Outline each uninfected red blood cell.
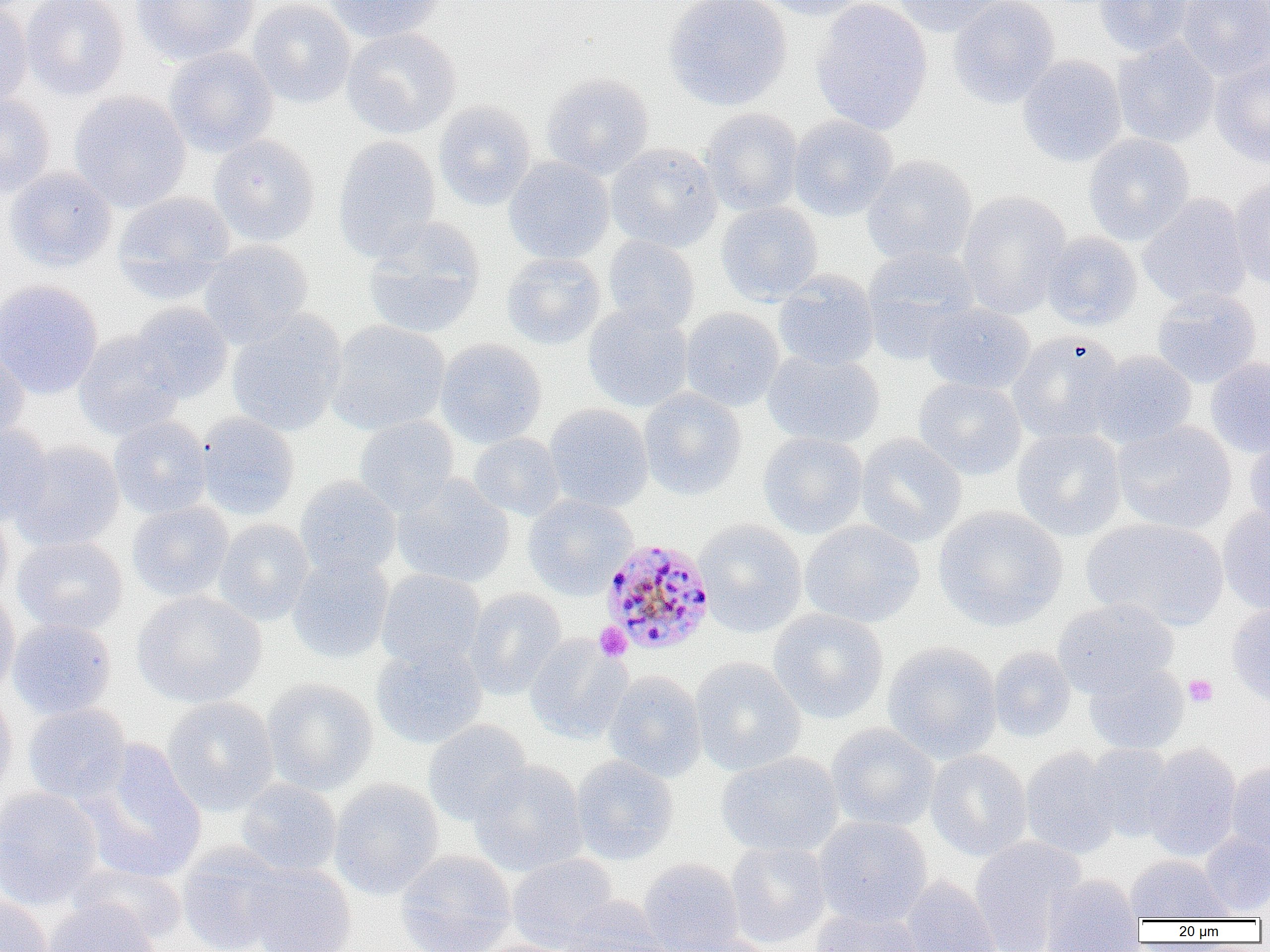

Approximate bounding boxes as [x1, y1, x2, y2] in pixels.
Uninfected red blood cells: [21, 0, 130, 101], [131, 0, 261, 65], [248, 0, 357, 108], [321, 0, 442, 43], [663, 0, 793, 111], [756, 0, 871, 21], [810, 0, 933, 135], [890, 0, 1009, 37], [948, 0, 1060, 108], [1093, 0, 1197, 57], [1176, 0, 1269, 79], [0, 2, 33, 109], [341, 27, 462, 139], [1112, 38, 1220, 148], [164, 46, 278, 157], [1018, 55, 1126, 167], [1210, 55, 1270, 168], [541, 72, 654, 179], [68, 91, 191, 212], [0, 94, 55, 199], [433, 100, 537, 211], [700, 107, 804, 216], [787, 115, 898, 221], [1083, 133, 1194, 245], [208, 134, 321, 247], [333, 135, 442, 261], [605, 143, 723, 252], [862, 154, 978, 266], [504, 156, 614, 265], [3, 166, 117, 273], [1230, 175, 1270, 288], [957, 190, 1072, 319], [113, 191, 236, 300], [1138, 193, 1252, 310], [716, 201, 823, 305], [362, 217, 486, 339], [1041, 231, 1142, 330], [602, 235, 700, 333], [198, 240, 313, 347], [862, 246, 980, 362], [501, 253, 606, 350], [773, 270, 880, 371], [0, 279, 103, 399], [1151, 289, 1261, 388], [128, 301, 234, 403], [922, 302, 1035, 394], [583, 304, 694, 413], [680, 307, 785, 411], [226, 309, 347, 437], [327, 320, 450, 435], [73, 330, 185, 440], [1007, 331, 1125, 444], [435, 339, 547, 448], [0, 342, 30, 444], [1089, 350, 1197, 449], [762, 351, 885, 448], [1205, 357, 1270, 458], [913, 377, 1027, 480], [638, 387, 747, 500], [544, 404, 653, 512], [195, 412, 300, 520], [353, 415, 460, 515], [109, 416, 212, 519], [1112, 421, 1237, 534], [0, 422, 54, 525], [1011, 428, 1127, 542], [1243, 430, 1270, 537], [757, 432, 869, 539], [468, 433, 565, 520], [856, 433, 967, 547], [9, 441, 125, 551], [392, 475, 515, 588], [294, 476, 401, 580], [523, 494, 636, 599], [127, 501, 234, 602], [0, 502, 13, 608], [1218, 503, 1270, 615], [933, 505, 1067, 631], [1081, 517, 1228, 630], [213, 519, 314, 625], [695, 519, 807, 637], [799, 520, 925, 628], [12, 535, 128, 635], [287, 554, 394, 663], [376, 569, 486, 671], [466, 588, 567, 699], [0, 590, 20, 702], [133, 591, 266, 708], [1053, 598, 1178, 698], [1226, 602, 1270, 708], [768, 608, 889, 724], [7, 618, 117, 720], [525, 635, 631, 744], [370, 641, 487, 749], [882, 641, 1003, 763], [988, 646, 1075, 743], [690, 657, 806, 776], [1084, 661, 1189, 755], [603, 669, 707, 783], [261, 678, 378, 796], [0, 687, 17, 799], [161, 696, 280, 816], [22, 703, 132, 805], [423, 720, 533, 826], [826, 723, 940, 832], [78, 743, 207, 885], [1084, 743, 1177, 842], [1143, 743, 1242, 862], [1020, 746, 1122, 861], [925, 749, 1032, 861], [717, 751, 844, 857], [570, 755, 678, 865], [469, 760, 588, 876], [1226, 761, 1270, 858], [236, 778, 342, 877], [328, 779, 444, 900], [0, 787, 104, 909], [813, 816, 932, 927], [1198, 831, 1270, 918], [969, 835, 1087, 952], [726, 841, 831, 948], [176, 842, 289, 952], [396, 850, 516, 952], [507, 853, 619, 951], [1124, 855, 1235, 922], [638, 858, 744, 952], [243, 861, 356, 952], [69, 862, 187, 946], [1041, 874, 1145, 951], [900, 876, 1001, 952], [0, 894, 53, 952], [559, 895, 667, 951], [42, 897, 161, 952], [810, 906, 925, 951], [668, 933, 779, 952], [469, 939, 581, 952].

slide-level diagnosis = Plasmodium malariae
image size = 1270×952 pixels
field of view = single
platelet locations = approximate bounding boxes as [x1, y1, x2, y2] in pixels: [594, 623, 632, 662], [1184, 674, 1218, 707]
modality = light microscopy
preparation = thin blood film
Plasmodium malariae-infected red blood cell locations = approximate bounding boxes as [x1, y1, x2, y2] in pixels: [600, 537, 716, 656]
magnification = 1000x